Locate every malaria parasite.
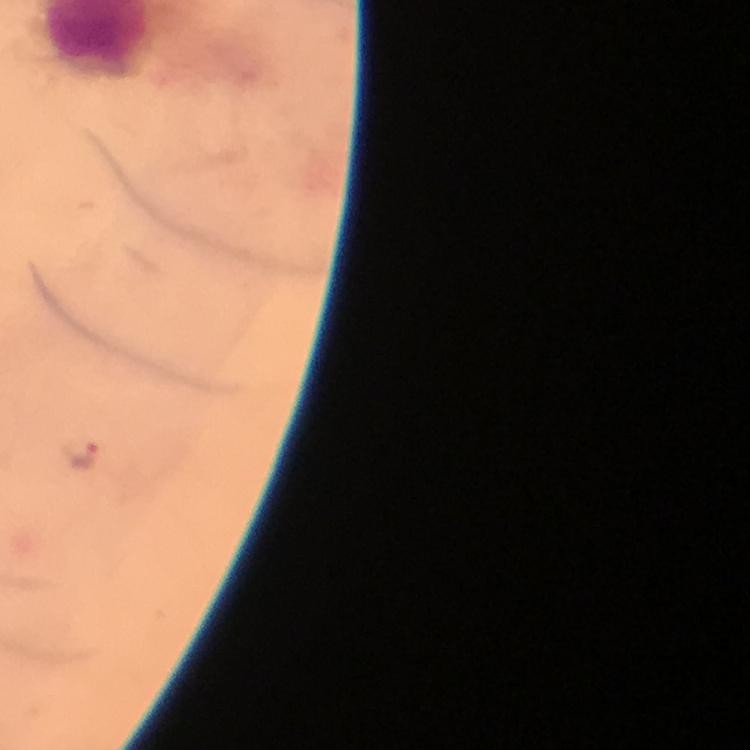

Approximate centers as [x, y] in pixels.
Malaria parasites: [82, 455].

100x magnification. Immersion oil applied. Photographed through the microscope with a smartphone camera. A crop from one field of view. Giemsa stain. Thick blood film. From a diagnostic examination for malaria. Image is 750×750 pixels.